Identify the parasite.
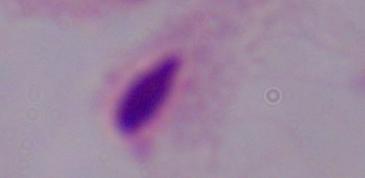
A trichomonad.

Micrograph. Captured at 1000x magnification.